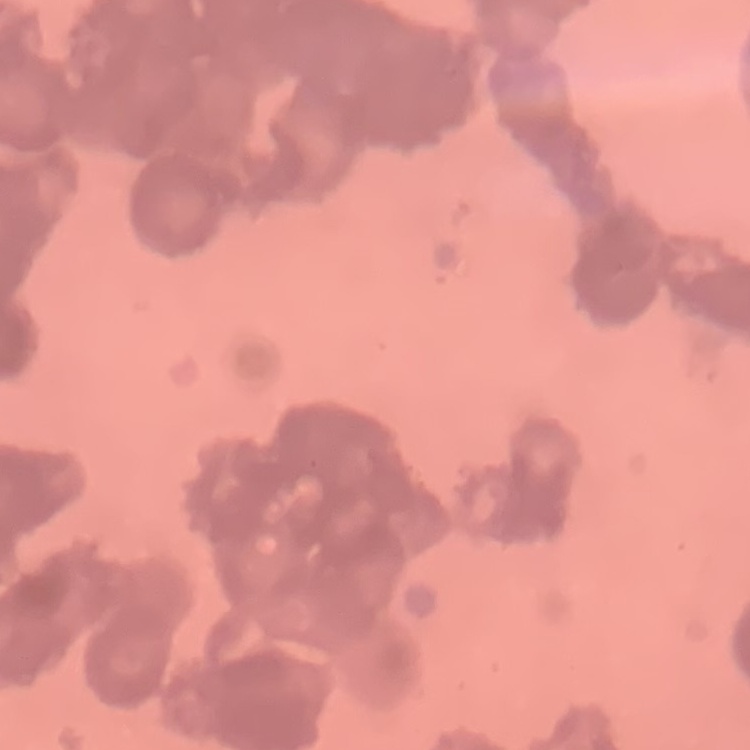
Summary:
  - Red blood cell morphology: rouleaux formation
  - Preparation: thin blood film
  - Image type: one tile cut from a larger photomicrograph
  - Stain: Field's or Giemsa